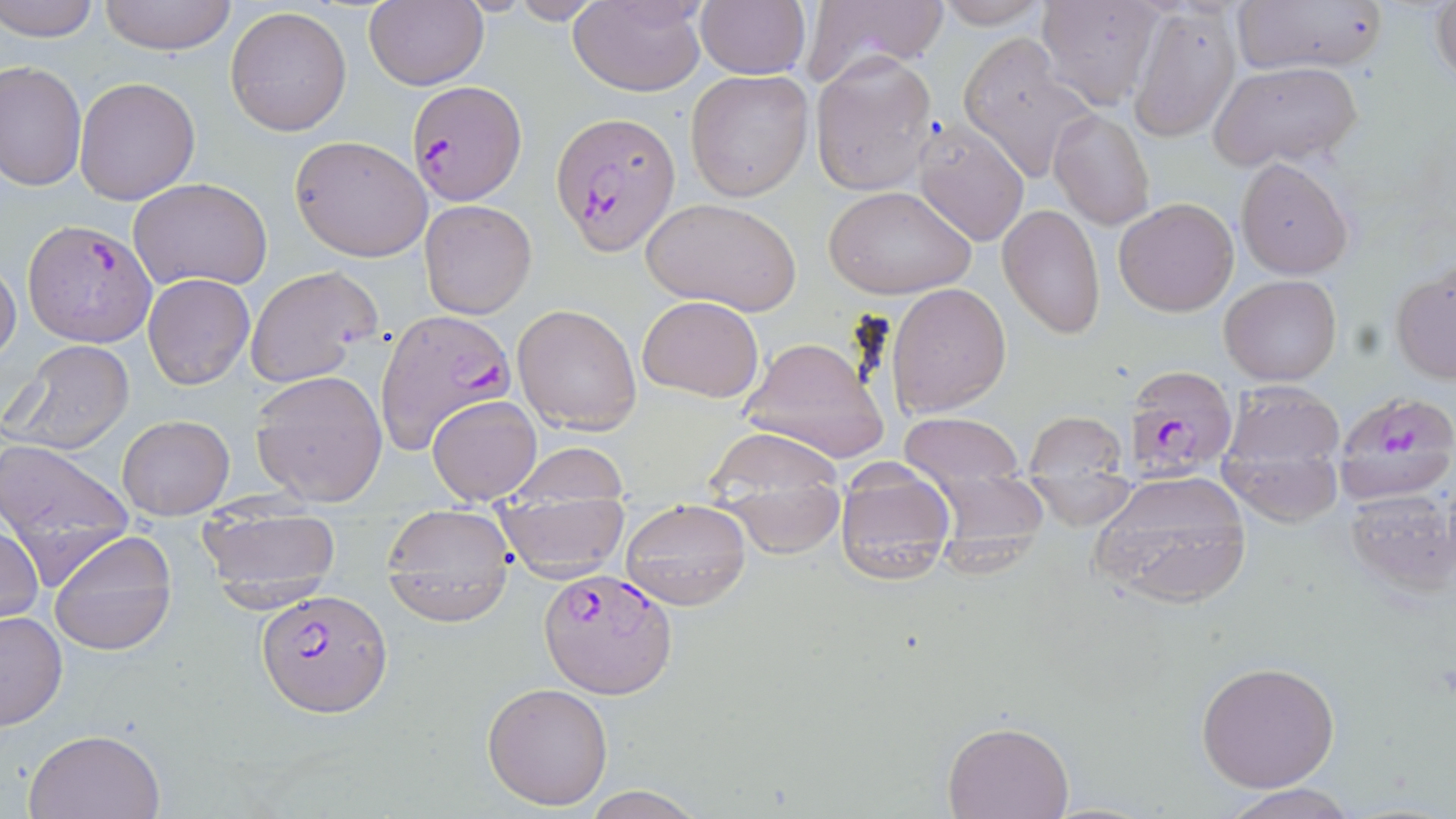
Summary:
  - Coordinate format: approximate bounding boxes as named x1/y1/x2/y2 corners in pixels
  - Uninfected red blood cell locations: (x1=1, y1=0, x2=102, y2=41), (x1=99, y1=0, x2=239, y2=55), (x1=363, y1=0, x2=488, y2=91), (x1=568, y1=0, x2=706, y2=95), (x1=934, y1=0, x2=1052, y2=28), (x1=1035, y1=0, x2=1169, y2=109), (x1=1231, y1=0, x2=1386, y2=77), (x1=1430, y1=0, x2=1456, y2=88), (x1=502, y1=1, x2=612, y2=24), (x1=694, y1=2, x2=809, y2=79), (x1=804, y1=2, x2=949, y2=81), (x1=1130, y1=4, x2=1242, y2=140), (x1=225, y1=5, x2=352, y2=137), (x1=959, y1=35, x2=1098, y2=181), (x1=811, y1=53, x2=938, y2=199), (x1=1, y1=60, x2=86, y2=190), (x1=1207, y1=62, x2=1364, y2=173), (x1=685, y1=69, x2=814, y2=200), (x1=75, y1=77, x2=201, y2=203), (x1=1050, y1=109, x2=1154, y2=230), (x1=912, y1=122, x2=1032, y2=247), (x1=289, y1=135, x2=433, y2=262), (x1=1237, y1=159, x2=1352, y2=276), (x1=129, y1=178, x2=273, y2=292), (x1=822, y1=184, x2=975, y2=300), (x1=640, y1=197, x2=802, y2=316), (x1=1114, y1=197, x2=1238, y2=316), (x1=419, y1=199, x2=537, y2=318), (x1=997, y1=203, x2=1104, y2=340), (x1=0, y1=263, x2=22, y2=367), (x1=245, y1=265, x2=381, y2=387), (x1=1390, y1=268, x2=1455, y2=384), (x1=142, y1=273, x2=254, y2=389), (x1=1220, y1=274, x2=1342, y2=387), (x1=886, y1=280, x2=1012, y2=417), (x1=637, y1=294, x2=764, y2=403), (x1=512, y1=301, x2=642, y2=435), (x1=740, y1=335, x2=889, y2=465), (x1=6, y1=339, x2=134, y2=455), (x1=249, y1=370, x2=387, y2=505), (x1=1218, y1=379, x2=1347, y2=489), (x1=427, y1=395, x2=541, y2=505), (x1=1024, y1=411, x2=1127, y2=478), (x1=898, y1=412, x2=1026, y2=480), (x1=118, y1=415, x2=233, y2=519), (x1=1218, y1=422, x2=1345, y2=526), (x1=701, y1=428, x2=849, y2=513), (x1=0, y1=440, x2=135, y2=575), (x1=505, y1=442, x2=630, y2=508), (x1=1088, y1=471, x2=1256, y2=606), (x1=921, y1=474, x2=1052, y2=564), (x1=1023, y1=475, x2=1136, y2=527), (x1=833, y1=480, x2=954, y2=581), (x1=494, y1=486, x2=630, y2=580), (x1=1343, y1=487, x2=1453, y2=595), (x1=620, y1=497, x2=751, y2=611), (x1=380, y1=504, x2=516, y2=626), (x1=199, y1=505, x2=345, y2=599), (x1=0, y1=521, x2=44, y2=627), (x1=48, y1=529, x2=177, y2=656), (x1=0, y1=610, x2=67, y2=731), (x1=1196, y1=660, x2=1340, y2=793), (x1=482, y1=681, x2=614, y2=810), (x1=942, y1=718, x2=1075, y2=818), (x1=22, y1=727, x2=166, y2=818), (x1=1219, y1=784, x2=1360, y2=819), (x1=580, y1=786, x2=706, y2=819)
  - Plasmodium falciparum-infected red blood cell locations: (x1=406, y1=78, x2=524, y2=207), (x1=552, y1=112, x2=680, y2=254), (x1=23, y1=220, x2=155, y2=348), (x1=377, y1=315, x2=518, y2=460), (x1=1121, y1=364, x2=1237, y2=481), (x1=1331, y1=394, x2=1456, y2=490), (x1=539, y1=568, x2=676, y2=696), (x1=258, y1=590, x2=391, y2=717)
  - Slide-level diagnosis: Plasmodium falciparum
  - Magnification: 1000x
  - Image size: 1456×819 pixels
  - Stain: May-Grünwald-Giemsa
  - Modality: optical microscopy
  - Field of view: one of a larger specimen
  - Preparation: thin blood smear